Give the extent of all uninfected red blood cells.
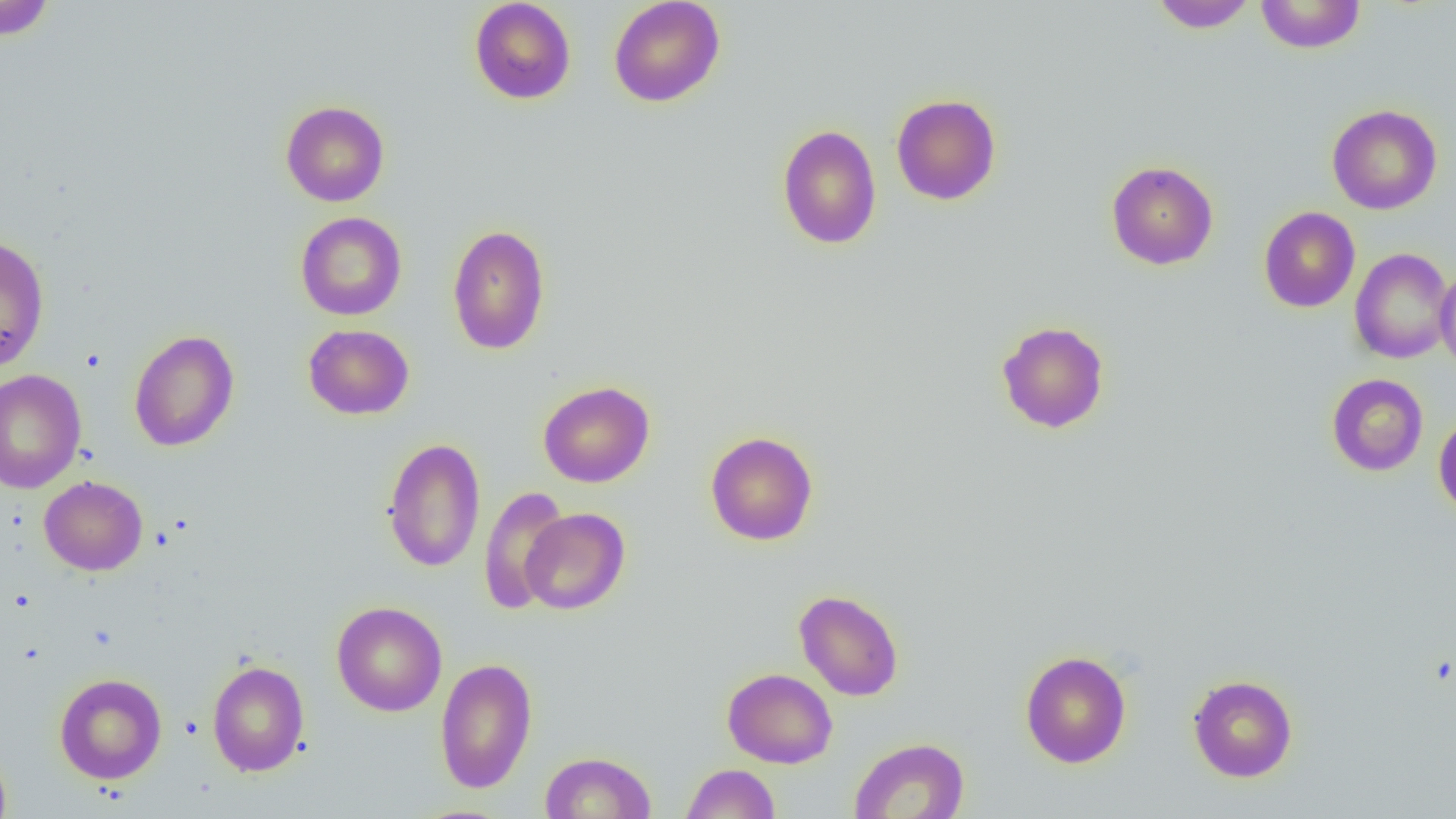

Approximate bounding boxes as named x1/y1/x2/y2 corners in pixels.
Uninfected red blood cells: (x1=469, y1=0, x2=576, y2=105), (x1=608, y1=0, x2=726, y2=107), (x1=1150, y1=0, x2=1257, y2=32), (x1=1255, y1=0, x2=1366, y2=53), (x1=0, y1=1, x2=57, y2=41), (x1=891, y1=93, x2=1002, y2=206), (x1=280, y1=100, x2=390, y2=207), (x1=1326, y1=104, x2=1442, y2=215), (x1=777, y1=124, x2=882, y2=249), (x1=1106, y1=161, x2=1218, y2=270), (x1=1259, y1=206, x2=1360, y2=312), (x1=295, y1=212, x2=407, y2=321), (x1=447, y1=223, x2=550, y2=356), (x1=0, y1=234, x2=50, y2=373), (x1=1349, y1=247, x2=1454, y2=364), (x1=1435, y1=265, x2=1456, y2=374), (x1=996, y1=320, x2=1110, y2=433), (x1=303, y1=324, x2=414, y2=420), (x1=129, y1=329, x2=240, y2=452), (x1=0, y1=369, x2=86, y2=494), (x1=1326, y1=373, x2=1428, y2=476), (x1=538, y1=380, x2=655, y2=487), (x1=1433, y1=413, x2=1456, y2=519), (x1=705, y1=430, x2=818, y2=545), (x1=382, y1=437, x2=486, y2=573), (x1=38, y1=475, x2=148, y2=575), (x1=478, y1=486, x2=572, y2=614), (x1=520, y1=507, x2=630, y2=615), (x1=794, y1=589, x2=904, y2=701), (x1=332, y1=601, x2=447, y2=717), (x1=1020, y1=649, x2=1132, y2=768), (x1=434, y1=657, x2=537, y2=794), (x1=207, y1=660, x2=310, y2=776), (x1=722, y1=668, x2=837, y2=768), (x1=54, y1=673, x2=167, y2=784), (x1=1187, y1=674, x2=1298, y2=782), (x1=849, y1=737, x2=969, y2=818), (x1=0, y1=742, x2=12, y2=819), (x1=541, y1=751, x2=656, y2=818), (x1=680, y1=763, x2=780, y2=818).

Summary:
  - Slide-level diagnosis: no evidence of blood parasites
  - Field of view: one of a larger specimen
  - Image size: 1456×819 pixels
  - Preparation: thin blood smear
  - Modality: optical microscopy
  - Magnification: 1000x